Report the malaria status of this cell.
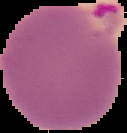

Parasitized.

From a thin blood film. Segmented cell region on a black background. Image is 127×133 pixels.